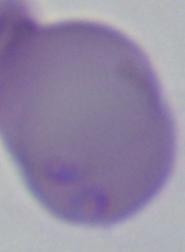

Summary:
  - Identification: Babesia
  - Magnification: 1000x
  - Modality: photomicrograph